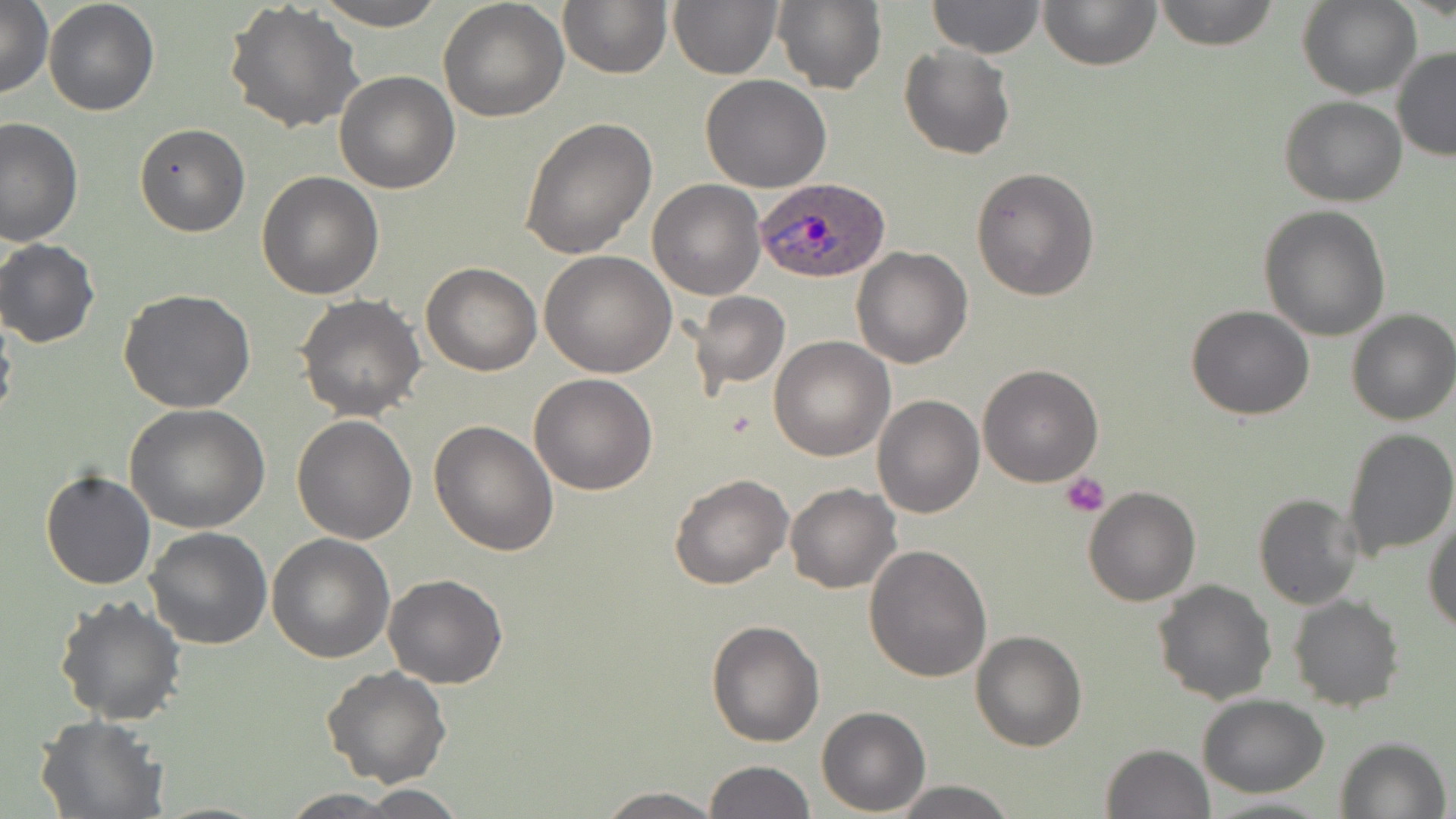

Summary:
  - Coordinate format: approximate bounding boxes as [x1, y1, x2, y2] in pixels
  - Plasmodium ovale-infected red blood cell locations: [754, 176, 892, 285]
  - Platelet locations: [1061, 472, 1110, 518]
  - Uninfected red blood cell locations: [43, 0, 160, 117], [224, 0, 366, 136], [313, 0, 446, 30], [438, 0, 569, 120], [558, 0, 671, 79], [667, 0, 781, 79], [772, 0, 888, 96], [1038, 0, 1162, 71], [1154, 0, 1281, 49], [1299, 0, 1418, 99], [927, 1, 1046, 58], [0, 2, 54, 100], [898, 45, 1016, 161], [1391, 47, 1456, 161], [333, 71, 459, 193], [700, 75, 832, 192], [1279, 96, 1407, 206], [520, 114, 657, 259], [1, 117, 82, 246], [134, 122, 250, 237], [970, 167, 1100, 301], [256, 171, 386, 299], [647, 179, 765, 300], [1259, 204, 1391, 341], [0, 238, 100, 348], [851, 246, 974, 368], [539, 250, 677, 377], [421, 262, 542, 376], [119, 289, 256, 412], [690, 291, 791, 394], [296, 293, 426, 422], [1187, 304, 1313, 421], [1345, 310, 1456, 426], [769, 337, 894, 461], [977, 363, 1104, 486], [529, 373, 658, 494], [873, 382, 1097, 501], [872, 394, 985, 518], [126, 404, 268, 535], [292, 414, 417, 543], [429, 421, 560, 556], [1339, 427, 1455, 563], [41, 468, 155, 591], [668, 472, 793, 590], [785, 483, 901, 594], [1083, 486, 1200, 606], [1252, 492, 1362, 609], [1424, 510, 1456, 632], [145, 526, 273, 648], [267, 532, 396, 662], [864, 543, 994, 683], [383, 574, 509, 689], [1151, 579, 1277, 703], [54, 595, 186, 724], [1289, 596, 1403, 713], [706, 620, 824, 747], [971, 630, 1086, 751], [322, 665, 452, 786], [1196, 693, 1329, 797], [817, 706, 930, 814], [33, 715, 169, 819], [1335, 736, 1452, 819], [1102, 744, 1214, 818], [704, 760, 816, 818], [890, 781, 1018, 817], [595, 787, 724, 818], [333, 788, 471, 817], [278, 790, 412, 818], [1199, 795, 1336, 818]
  - Slide-level diagnosis: Plasmodium ovale
  - Stain: May-Grünwald-Giemsa
  - Image size: 1456×819 pixels
  - Magnification: 1000x
  - Modality: light microscopy
  - Preparation: thin blood smear
  - Field of view: single